Report the malaria status of this cell.
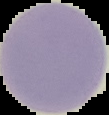

Uninfected.

Image is 109×115 pixels. Cell region segmented out of the field of view; the surrounding area is masked to black. From a thin blood film.